Name the parasite shown.
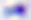

This is Toxoplasma gondii.

magnification = 400x
modality = photomicrograph